Identify the blood parasite species.
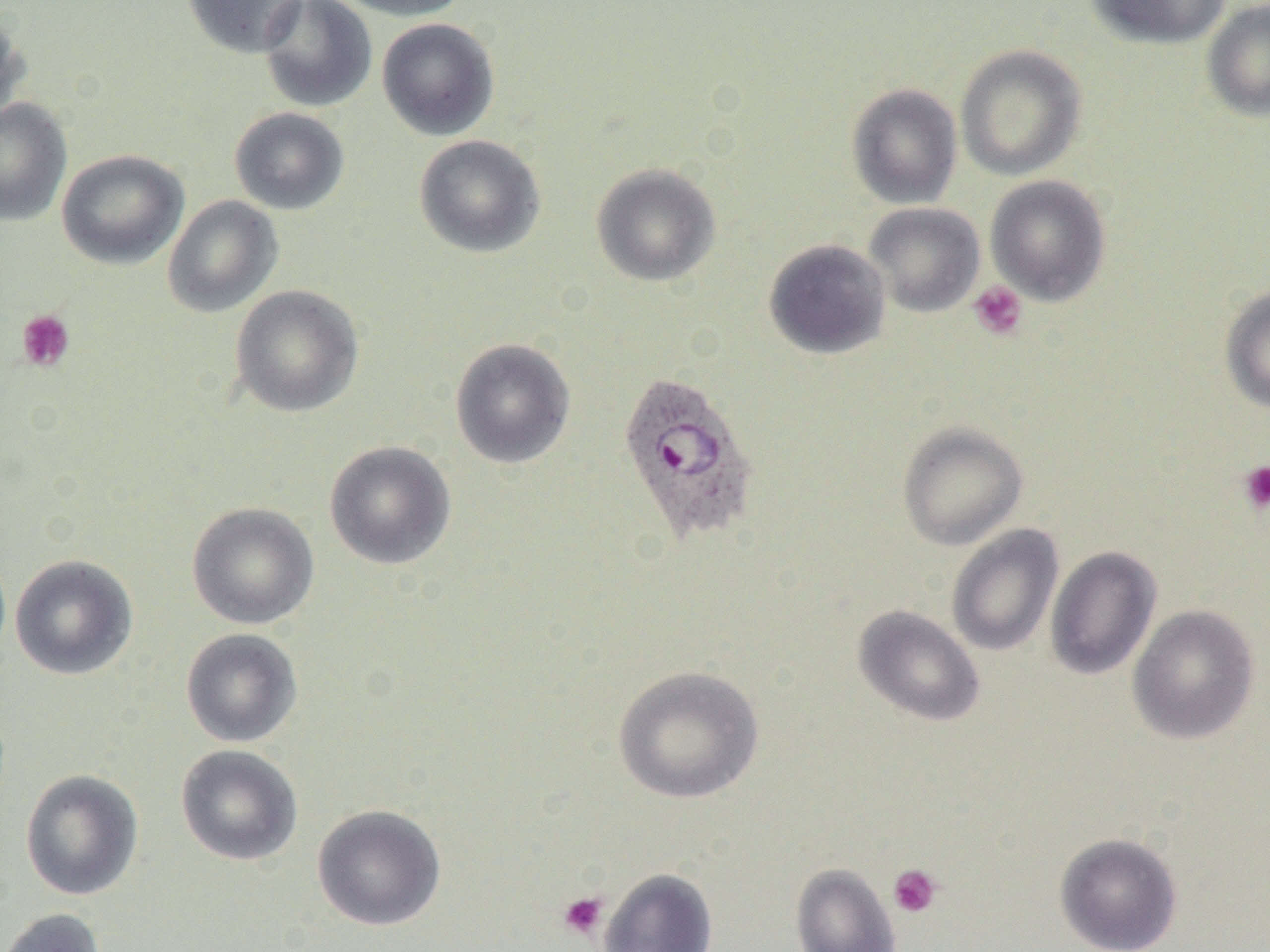
Plasmodium ovale.

Approximate bounding boxes as (x1,y1)-(x2,y2) corner pairs in pixels. Platelet locations: (968,280)-(1028,340), (16,309)-(75,372), (1238,460)-(1270,514), (887,864)-(942,918), (558,891)-(608,940). Plasmodium ovale-infected red blood cell locations: (616,372)-(761,545). Uninfected red blood cell locations: (182,0)-(307,58), (259,0)-(378,112), (331,0)-(472,21), (1087,0)-(1231,49), (1201,0)-(1270,122), (0,5)-(31,126), (377,18)-(500,141), (955,44)-(1087,181), (846,83)-(962,209), (0,97)-(72,227), (229,107)-(350,215), (414,134)-(546,258), (56,149)-(189,270), (591,163)-(721,286), (984,175)-(1112,306), (161,195)-(283,318), (863,202)-(986,317), (763,238)-(891,359), (229,284)-(365,418), (1219,285)-(1270,414), (450,338)-(576,469), (896,421)-(1028,550), (324,440)-(456,570), (187,502)-(319,630), (946,524)-(1064,657), (1044,546)-(1161,680), (10,554)-(138,680), (1127,604)-(1260,744), (852,605)-(985,727), (180,628)-(302,747), (612,664)-(765,803), (175,744)-(303,866), (20,769)-(143,900), (312,804)-(446,931), (1054,832)-(1183,951), (790,862)-(902,952), (598,868)-(718,952), (1,907)-(105,952). Thin blood film. Optical microscopy. One field of a larger specimen. Captured at 1000x magnification. Image is 1270×952 pixels.